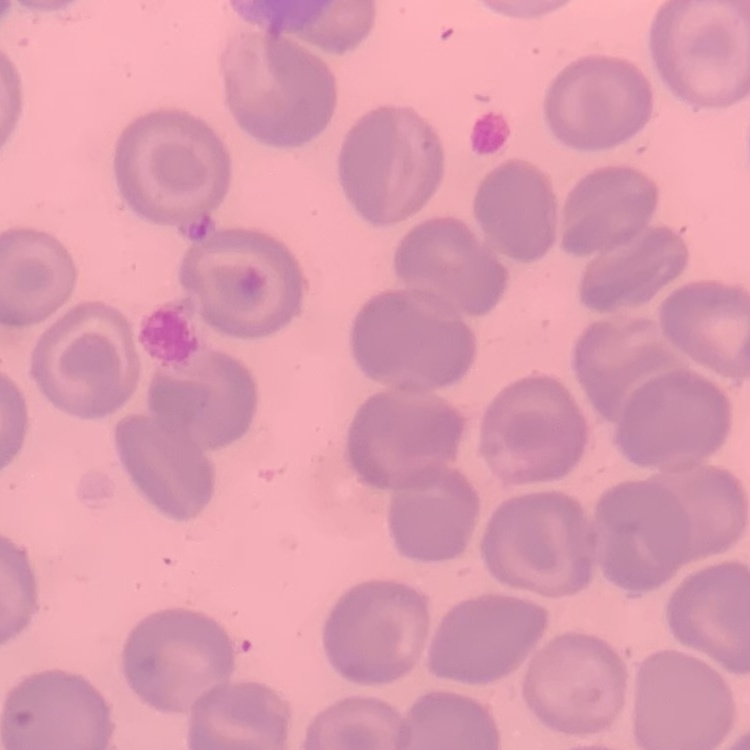
The erythrocytes show no rouleaux formation. Thin blood film. One tile cut from a larger photomicrograph. Stained with either Field's or Giemsa.